Locate every Plasmodium parasite.
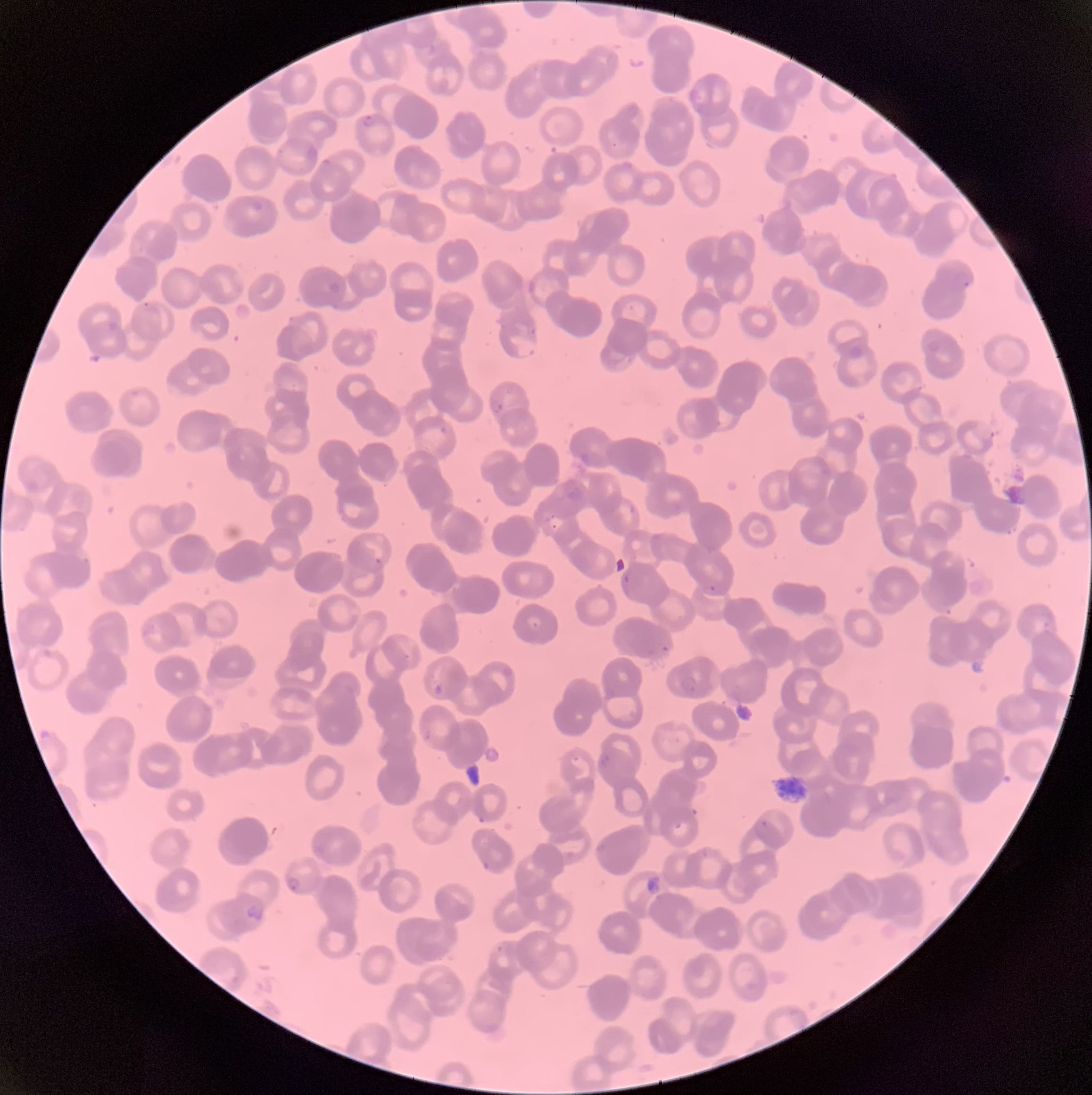
Approximate bounding boxes as (x1,y1)-(x2,y2) corner pairs in pixels.
Plasmodium parasites: (363,114)-(374,127), (955,269)-(971,287), (510,339)-(539,357), (491,401)-(503,414), (975,420)-(995,440), (372,555)-(385,567), (622,571)-(631,586), (709,584)-(717,592), (659,644)-(671,654), (678,675)-(697,693), (434,685)-(444,694), (600,755)-(610,765), (760,821)-(770,829), (289,875)-(300,891), (246,903)-(263,920).

Summary:
  - Red blood cell morphology: rouleaux formation
  - Modality: optical microscopy
  - Image size: 1092×1095 pixels
  - Preparation: thin blood film